Describe the morphology of the red blood cells.
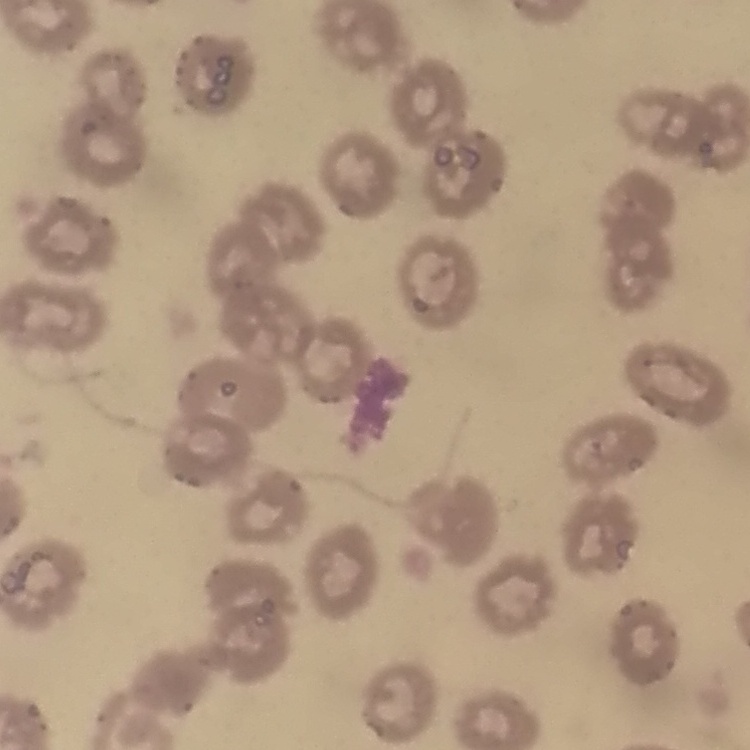
They show no rouleaux formation.

Summary:
  - Preparation: thin peripheral smear
  - Stain: Field's or Giemsa
  - Image type: one tile cut from a larger photomicrograph